Locate malaria parasites and identify their life-cycle stages.
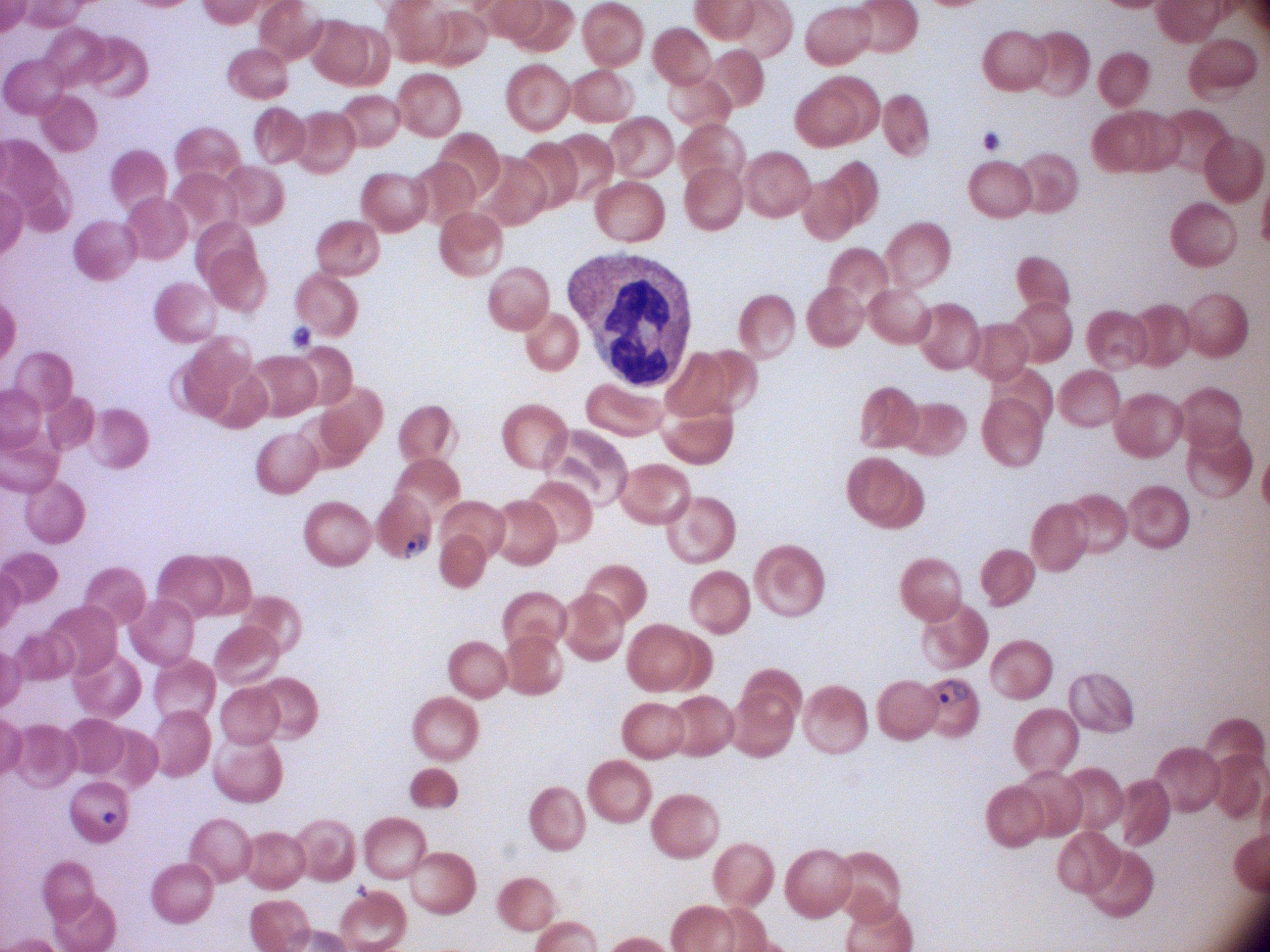

Approximate bounding boxes as (x1,y1)-(x2,y2) corner pairs in pixels, from the source annotation, which is not necessarily exhaustive.
Ring forms: (399,528)-(432,564), (928,673)-(973,711).

Summary:
  - Image size: 1270×952 pixels
  - Preparation: thin blood film
  - Field of view: one from this slide
  - Stain: Giemsa
  - Species: Plasmodium falciparum
  - Magnification: 100x
  - Microscope: Leica DM2000 with built-in camera